Assess this cell for malaria.
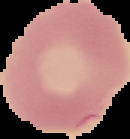
It is uninfected.

preparation = thin blood film
image size = 130×139 pixels
image type = cell region segmented out of the field of view; surrounding area masked to black